State which parasite is depicted.
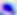
Toxoplasma gondii.

Summary:
  - Magnification: 400x
  - Modality: photomicrograph